Outline each blood parasite and name the species.
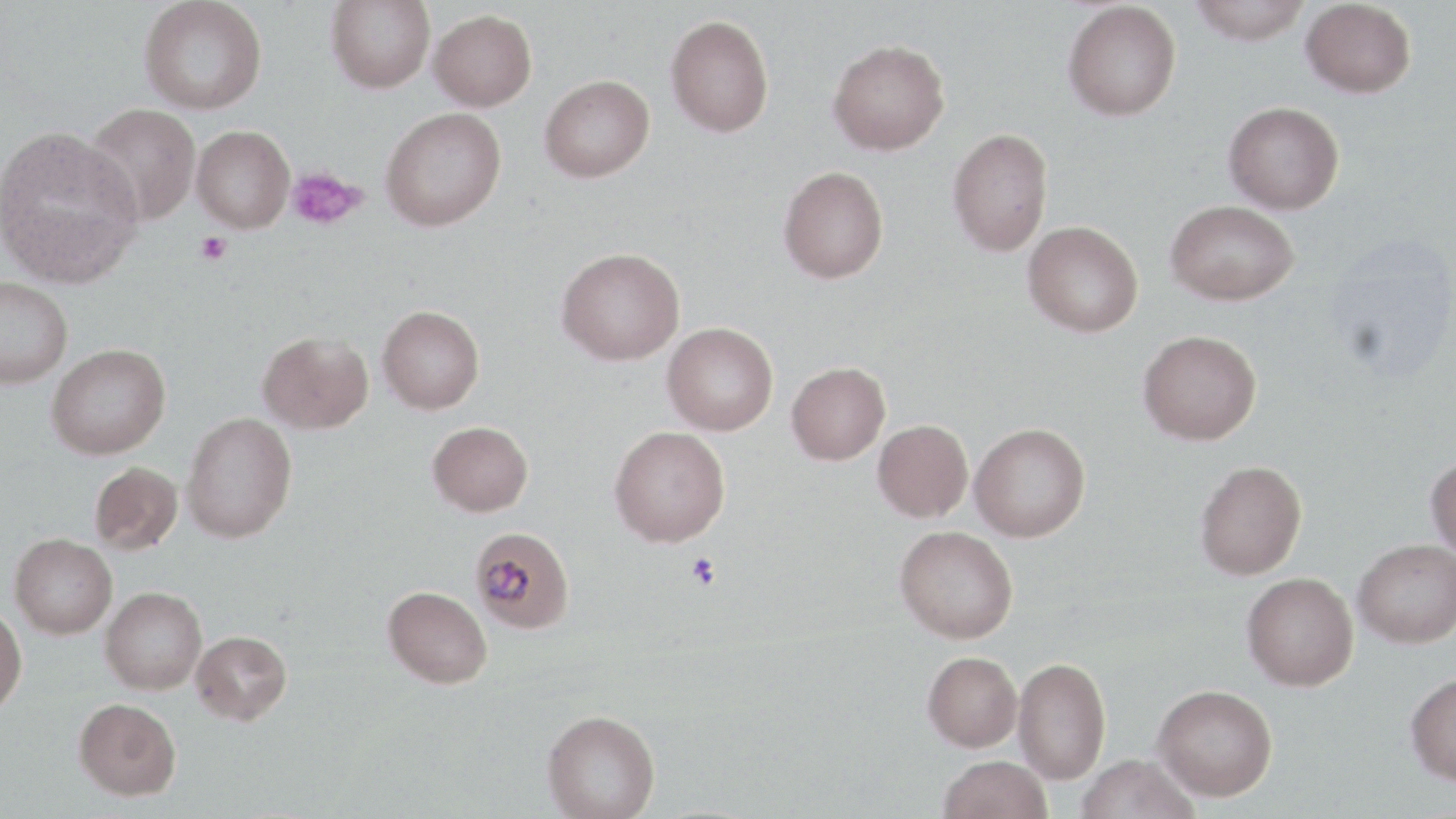
Approximate bounding boxes as [x1, y1, x2, y2] in pixels.
Plasmodium malariae-infected red blood cells: [470, 526, 573, 633].
No Plasmodium falciparum, Plasmodium ovale, Plasmodium vivax, Babesia divergens, or Trypanosoma brucei observed.

Summary:
  - Uninfected red blood cell locations: [139, 0, 268, 115], [326, 0, 435, 93], [1187, 0, 1313, 44], [1301, 0, 1416, 98], [1062, 1, 1182, 121], [429, 9, 537, 111], [665, 14, 774, 137], [828, 39, 950, 155], [539, 74, 654, 182], [1223, 101, 1345, 214], [84, 103, 200, 226], [380, 107, 506, 231], [0, 125, 143, 287], [192, 125, 295, 233], [948, 128, 1053, 256], [778, 165, 889, 283], [1164, 200, 1300, 305], [1023, 220, 1143, 337], [1325, 236, 1456, 382], [556, 247, 685, 365], [0, 276, 72, 388], [377, 305, 485, 414], [662, 323, 778, 435], [1138, 329, 1262, 445], [257, 330, 373, 433], [46, 343, 171, 460], [786, 362, 890, 465], [180, 411, 297, 543], [873, 420, 973, 522], [427, 421, 533, 516], [969, 423, 1090, 542], [609, 425, 730, 547], [1425, 454, 1456, 561], [1194, 460, 1307, 580], [89, 462, 183, 555], [894, 526, 1018, 643], [9, 534, 117, 638], [1353, 539, 1456, 647], [1241, 572, 1358, 690], [383, 586, 493, 688], [100, 587, 207, 694], [0, 604, 27, 715], [190, 630, 292, 725], [922, 651, 1022, 751], [1013, 656, 1111, 784], [1404, 673, 1456, 785], [1153, 684, 1277, 800], [74, 697, 181, 800], [542, 709, 661, 818], [938, 754, 1052, 819], [1075, 754, 1200, 819]
  - Platelet locations: [286, 167, 367, 230], [195, 232, 232, 266], [686, 552, 720, 591]
  - Slide-level diagnosis: Plasmodium malariae
  - Stain: May-Grünwald-Giemsa
  - Image size: 1456×819 pixels
  - Magnification: 1000x
  - Field of view: single
  - Modality: light microscopy
  - Preparation: thin blood film